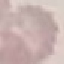
Summary:
  - Malaria status: uninfected
  - Preparation: thin smear
  - Capture: smartphone camera at the microscope eyepiece
  - Image type: automatically extracted cell patch, resized to 64 × 64 pixels
  - Stain: Giemsa